Locate every Plasmodium parasite.
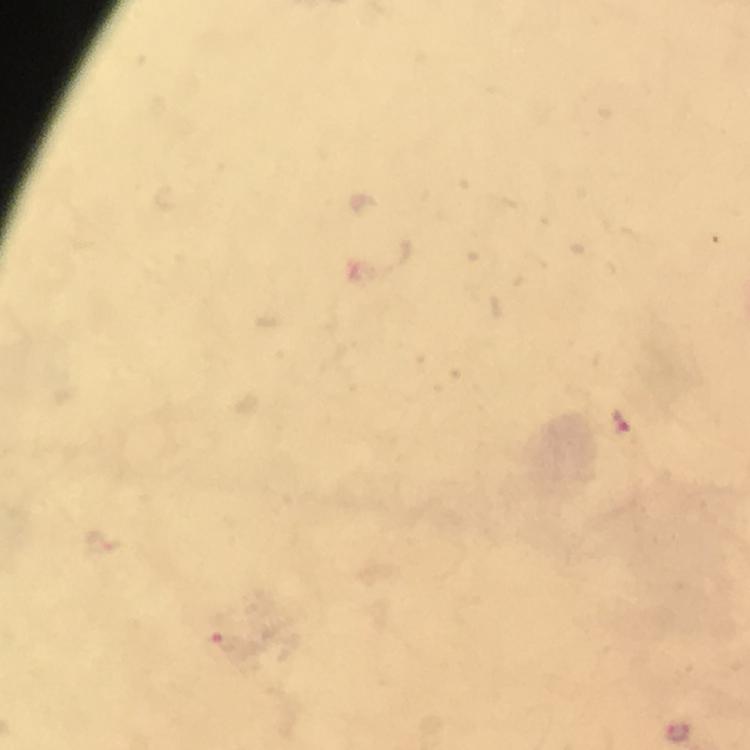
Approximate centers as {x, y} in pixels.
Plasmodium parasites: {620, 422}, {228, 643}.

Giemsa-stained preparation. A crop from one field of view. From a malaria diagnostic workup. Thick smear. At 100x magnification. Image is 750×750 pixels. Smartphone photograph taken through a microscope. Immersion oil was used.